State which parasite is depicted.
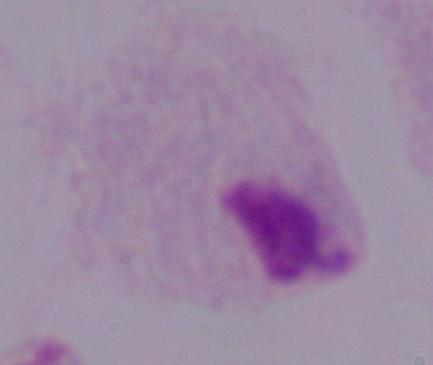

A trichomonad.

modality = photomicrograph
magnification = 1000x